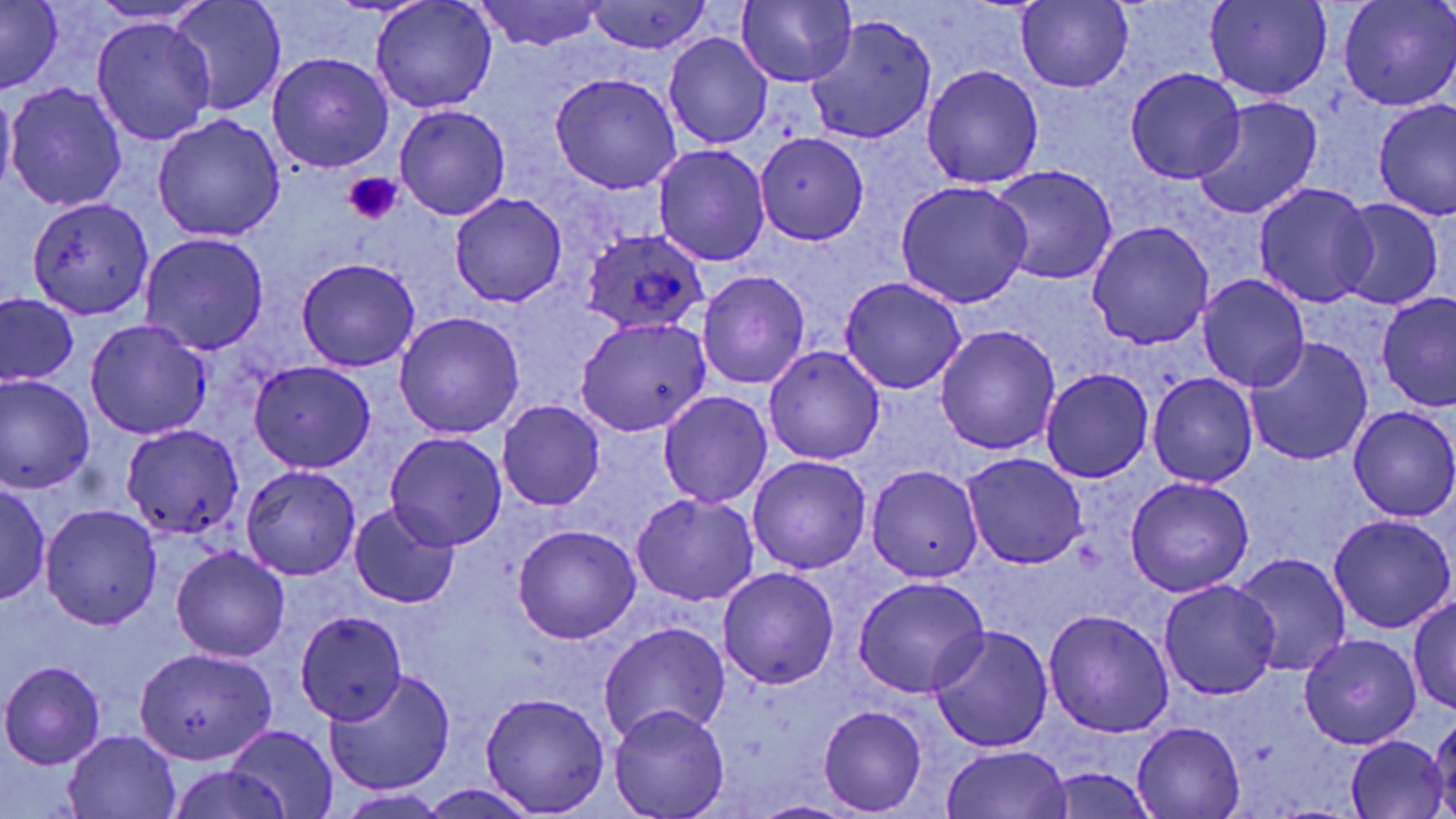

slide-level diagnosis = Plasmodium ovale
uninfected red blood cell locations = approximate bounding boxes as (x1, y1, x2, y2) in pixels: (370, 0, 496, 113), (1204, 0, 1331, 101), (1340, 0, 1454, 110), (473, 1, 609, 52), (734, 1, 857, 87), (1017, 1, 1133, 92), (0, 2, 62, 92), (587, 2, 713, 55), (167, 3, 285, 113), (807, 15, 936, 143), (90, 17, 215, 145), (665, 33, 772, 148), (267, 52, 394, 172), (922, 64, 1044, 188), (1125, 68, 1248, 184), (551, 72, 682, 194), (6, 82, 128, 212), (0, 84, 17, 198), (1193, 98, 1322, 221), (1373, 101, 1456, 219), (395, 104, 510, 219), (153, 115, 285, 242), (754, 132, 869, 245), (653, 144, 770, 266), (989, 165, 1118, 287), (896, 181, 1032, 308), (1254, 183, 1378, 309), (450, 193, 567, 308), (27, 195, 154, 321), (1335, 199, 1443, 310), (1087, 222, 1214, 349), (141, 233, 269, 354), (296, 257, 420, 371), (697, 270, 811, 390), (1199, 273, 1309, 392), (839, 277, 967, 395), (1376, 291, 1455, 413), (1, 292, 79, 387), (394, 311, 525, 438), (576, 318, 711, 438), (86, 319, 213, 438), (934, 324, 1061, 455), (1246, 336, 1372, 466), (764, 345, 885, 465), (250, 360, 375, 471), (1042, 368, 1153, 483), (1148, 374, 1257, 488), (0, 375, 96, 495), (659, 391, 772, 509), (498, 400, 606, 511), (1348, 405, 1456, 522), (123, 427, 244, 540), (384, 431, 508, 551), (963, 452, 1087, 568), (748, 456, 871, 573), (241, 465, 361, 581), (865, 465, 984, 582), (1125, 477, 1255, 597), (1, 482, 50, 606), (631, 492, 759, 606), (40, 503, 164, 629), (349, 503, 461, 609), (1328, 514, 1455, 634), (513, 524, 640, 644), (170, 546, 290, 661), (1232, 554, 1351, 677), (718, 567, 838, 689), (853, 578, 989, 698), (1159, 578, 1280, 701), (1410, 596, 1456, 716), (1043, 609, 1173, 737), (297, 611, 406, 724), (598, 621, 730, 744), (929, 625, 1055, 753), (1298, 633, 1422, 750), (137, 648, 276, 764), (0, 661, 107, 769), (324, 667, 456, 797), (480, 692, 609, 816), (818, 705, 926, 814), (609, 706, 729, 819), (1430, 716, 1456, 815), (1132, 720, 1244, 818), (225, 725, 340, 818), (63, 731, 181, 818), (1346, 734, 1447, 817), (941, 745, 1073, 819), (168, 766, 293, 819), (1047, 767, 1156, 819), (419, 784, 539, 819), (337, 790, 451, 818), (749, 800, 859, 819)
magnification = 1000x
stain = May-Grünwald-Giemsa
platelet locations = approximate bounding boxes as (x1, y1, x2, y2) in pixels: (343, 172, 402, 224)
preparation = thin blood film
modality = optical microscopy
image size = 1456×819 pixels
field of view = one of a larger specimen
Plasmodium ovale-infected red blood cell locations = approximate bounding boxes as (x1, y1, x2, y2) in pixels: (581, 230, 708, 335)